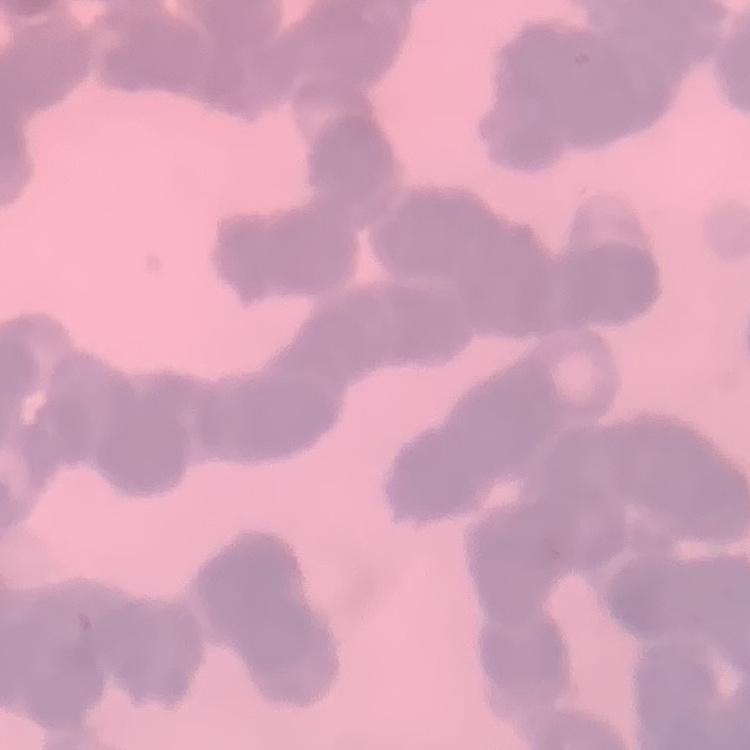
Summary:
  - Erythrocyte morphology: rouleaux formation
  - Stain: Field's or Giemsa
  - Preparation: thin peripheral smear
  - Image type: one tile cut from a larger photomicrograph